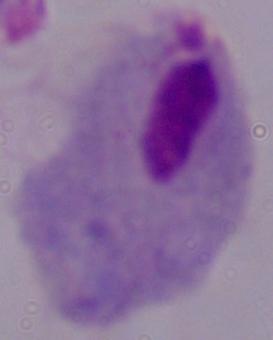

modality = photomicrograph
magnification = 1000x
identification = trichomonad